Point out each Plasmodium parasite and each leukocyte.
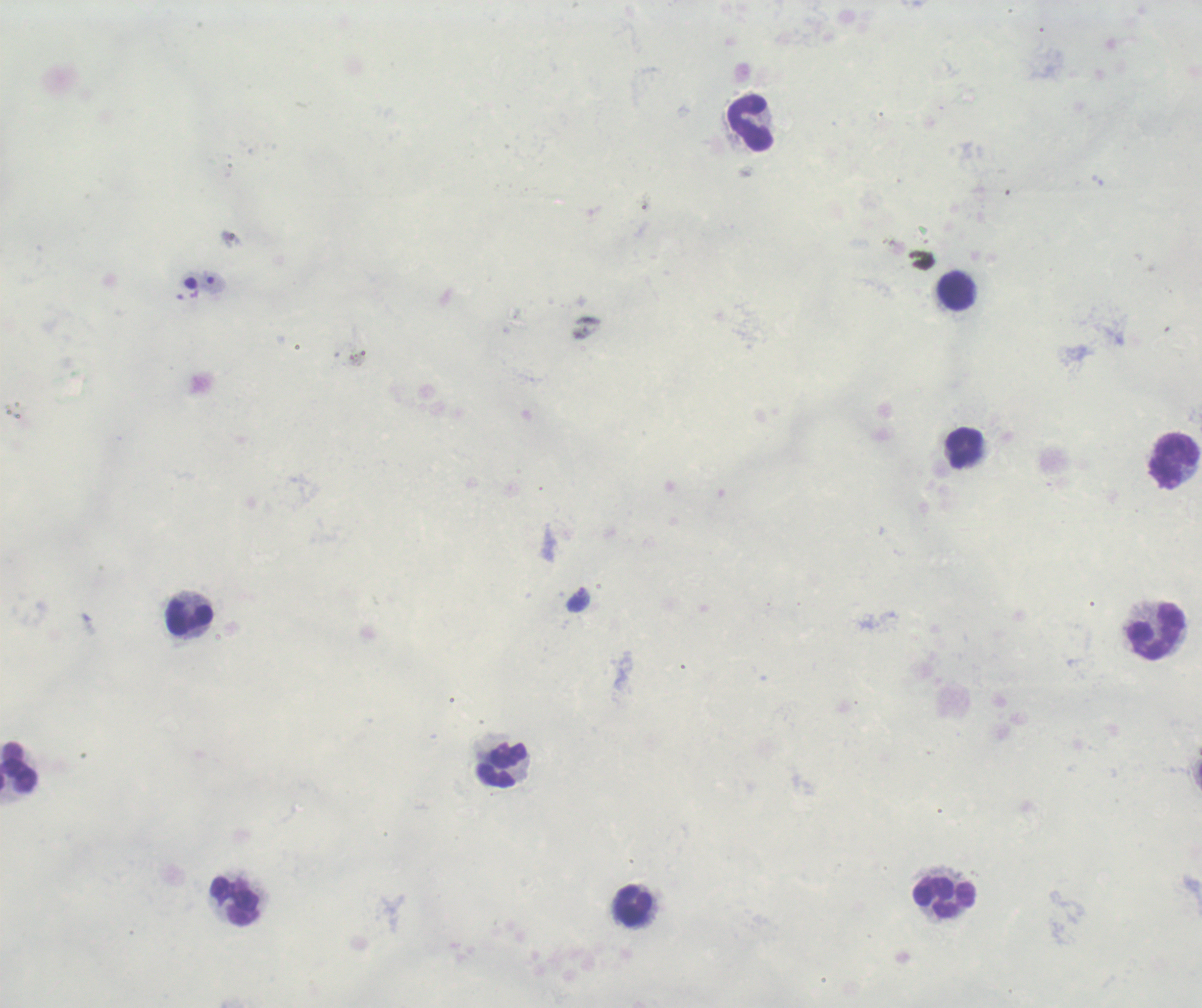
Approximate object centers, in pixels from the top-left corner.
Trophozoites: (x=578, y=599).
No schizont or gametocyte forms observed.
Leukocytes: (x=750, y=126), (x=956, y=293), (x=964, y=448), (x=1176, y=462), (x=188, y=618), (x=1155, y=633), (x=501, y=765), (x=19, y=768), (x=944, y=897), (x=234, y=901), (x=633, y=907).

Image is 1202×1008 pixels. Thick blood film. Single field of view. 100x magnification. Background quality: poor. Previously used in a real diagnosis. Romanowsky stain.